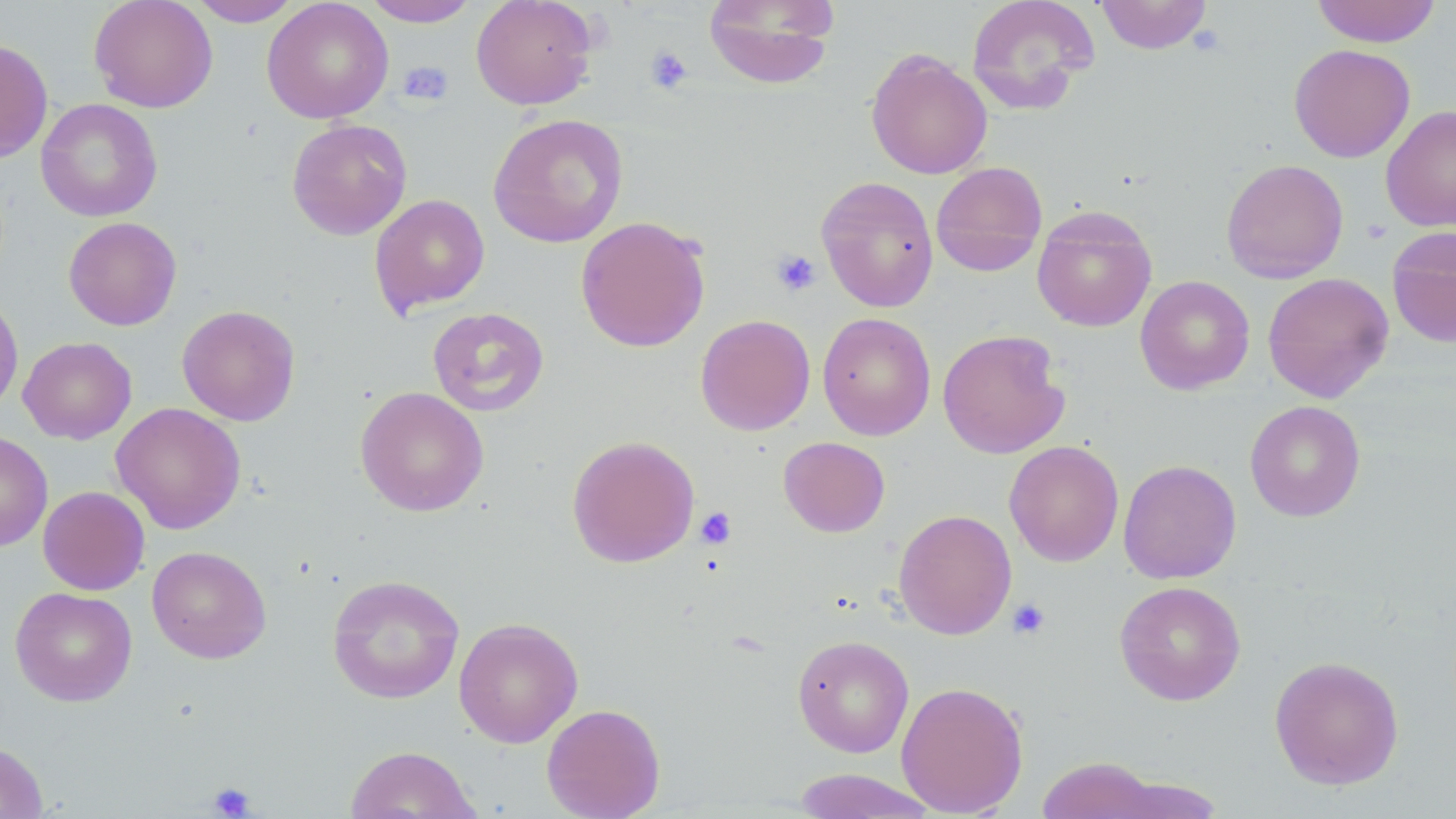

{
  "slide_level_diagnosis": "negative for blood parasites",
  "preparation": "thin blood smear",
  "field_of_view": "single",
  "platelet_locations": "approximate bounding boxes as (x1,y1)-(x2,y2) corner pairs in pixels: (646,46)-(693,94), (399,60)-(454,106), (1362,219)-(1392,244), (771,249)-(822,298), (695,507)-(737,549), (1007,598)-(1051,640), (208,782)-(257,818)",
  "stain": "May-Grünwald-Giemsa",
  "magnification": "1000x",
  "image_size": "1456×819 pixels",
  "uninfected_red_blood_cell_locations": "approximate bounding boxes as (x1,y1)-(x2,y2) corner pairs in pixels: (89,0)-(218,113), (188,0)-(303,26), (262,0)-(394,124), (362,0)-(480,27), (470,0)-(597,110), (704,0)-(837,89), (965,0)-(1101,115), (1095,0)-(1213,54), (1312,0)-(1442,48), (0,39)-(53,163), (1289,44)-(1415,162), (865,48)-(992,180), (36,98)-(163,222), (1381,105)-(1456,232), (488,113)-(628,248), (286,119)-(412,240), (1221,158)-(1349,284), (930,161)-(1048,277), (816,175)-(939,312), (370,194)-(490,316), (1032,206)-(1157,332), (575,215)-(711,353), (63,216)-(182,331), (1386,227)-(1456,347), (1262,272)-(1394,402), (1135,275)-(1255,394), (0,292)-(23,416), (177,305)-(301,426), (427,307)-(549,417), (818,312)-(936,440), (695,314)-(815,435), (937,329)-(1070,459), (18,336)-(137,444), (355,386)-(489,516), (1244,400)-(1366,522), (111,402)-(246,534), (0,430)-(53,552), (566,435)-(700,568), (778,436)-(890,537), (1004,440)-(1124,567), (1118,460)-(1241,584), (38,486)-(150,595), (893,509)-(1017,640), (147,545)-(271,664), (327,574)-(465,705), (1114,580)-(1247,706), (10,587)-(137,706), (453,616)-(583,748), (792,634)-(914,758), (1269,655)-(1404,790), (896,680)-(1028,817), (541,702)-(665,819), (0,741)-(48,818), (344,745)-(481,819), (1037,757)-(1166,818), (791,768)-(938,819)",
  "modality": "light microscopy"
}